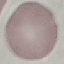 Malaria status: uninfected. Photographed with a smartphone camera at the microscope eyepiece. Thin blood film. Cell patch, automatically extracted from a larger field of view and resized to 64 × 64 pixels. Giemsa-stained preparation.